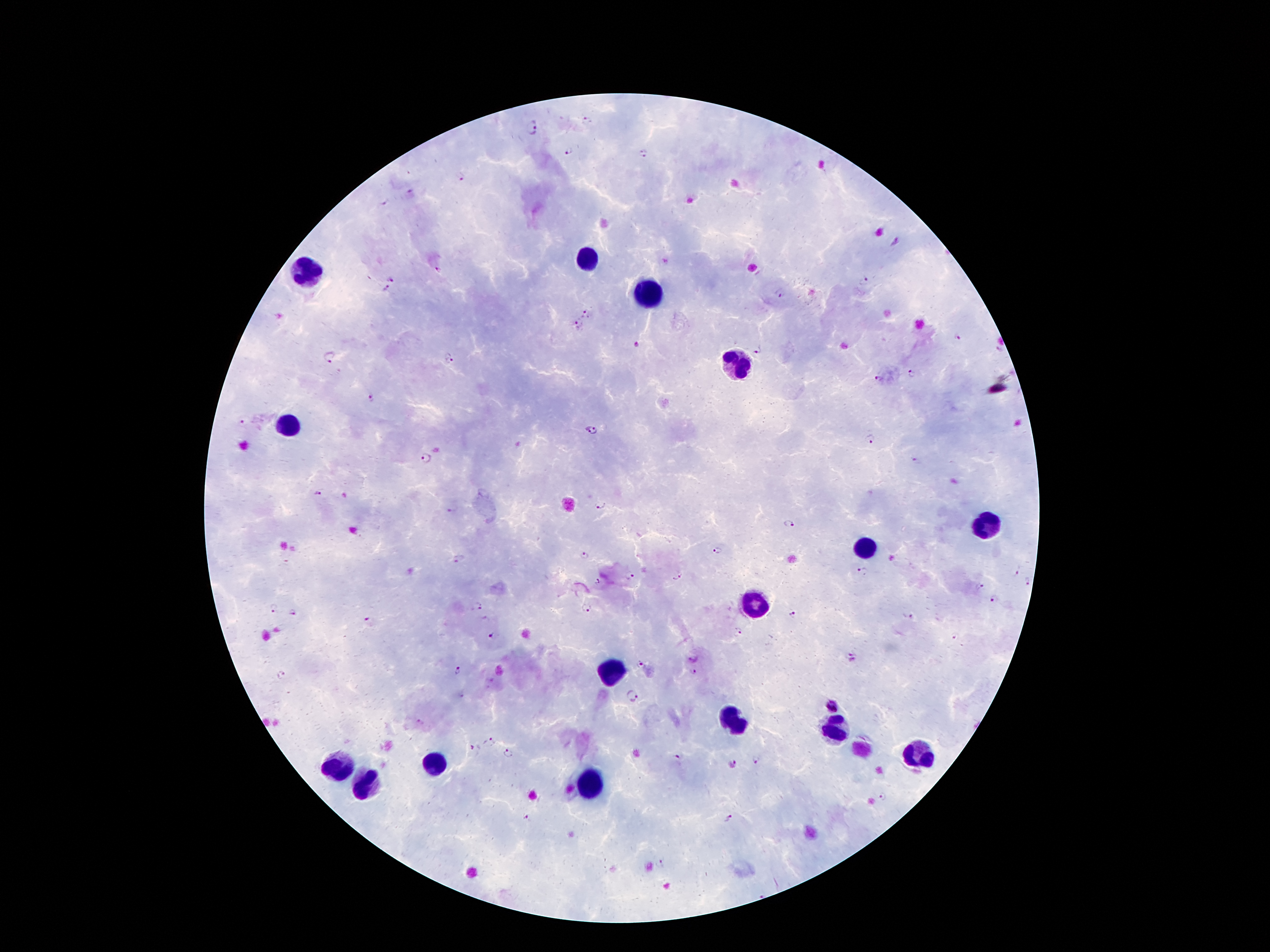
Approximate centers as {x, y} in pixels. Leukocyte locations: {587, 259}, {308, 268}, {647, 294}, {736, 362}, {289, 426}, {985, 526}, {866, 548}, {753, 607}, {608, 673}, {733, 722}, {834, 727}, {918, 757}, {436, 765}, {335, 768}, {589, 786}, {365, 787}. Plasmodium parasite locations: {586, 120}, {534, 128}, {569, 151}, {644, 154}, {461, 178}, {410, 191}, {384, 204}, {895, 244}, {391, 278}, {863, 281}, {386, 289}, {777, 295}, {587, 314}, {577, 326}, {960, 337}, {637, 346}, {757, 352}, {329, 358}, {449, 359}, {913, 373}, {879, 378}, {372, 399}, {243, 423}, {594, 429}, {870, 440}, {427, 458}, {916, 461}, {319, 495}, {600, 505}, {453, 510}, {790, 523}, {717, 551}, {585, 555}, {460, 560}, {863, 572}, {1016, 573}, {630, 576}, {678, 578}, {596, 580}, {1028, 582}, {979, 585}, {995, 600}, {480, 607}, {273, 609}, {586, 609}, {293, 612}, {793, 614}, {910, 616}, {369, 621}, {738, 631}, {491, 636}, {955, 636}, {690, 659}, {853, 659}, {638, 665}, {458, 669}, {693, 672}, {281, 675}, {463, 695}, {631, 695}, {833, 707}, {420, 721}, {490, 741}, {471, 749}, {507, 754}, {677, 758}, {756, 761}, {733, 763}, {883, 796}, {526, 818}, {729, 818}, {662, 863}. Smartphone photograph taken through the microscope eyepiece. One field from this slide. Patient malaria status: positive for Plasmodium falciparum. Giemsa stain. Image is 1270×952 pixels. Thick blood film. 100x magnification.